State which parasite is depicted.
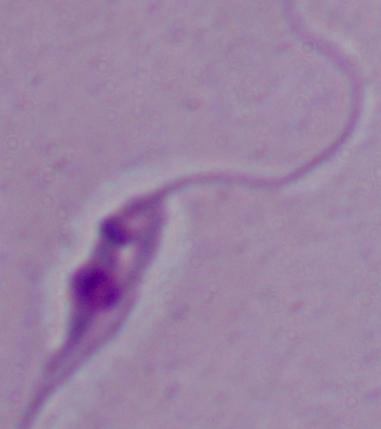
Leishmania.

1000x magnification. Photomicrograph.